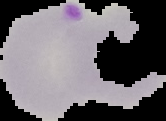
Summary:
  - Preparation: thin blood smear
  - Result: malaria parasites detected
  - Image size: 166×121 pixels
  - Image type: cell region segmented out of the field of view; surrounding area masked to black